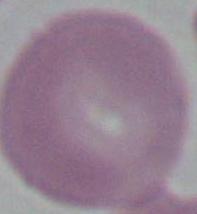

{
  "modality": "micrograph",
  "identification": "erythrocyte",
  "magnification": "1000x"
}